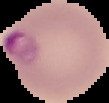
Summary:
  - Image size: 109×103 pixels
  - Preparation: thin blood film
  - Result: malaria parasites identified
  - Image type: cell region segmented out of the field of view; surrounding area masked to black